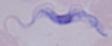

identification = trypanosome
modality = micrograph
magnification = 1000x